Assess the morphology of the erythrocytes.
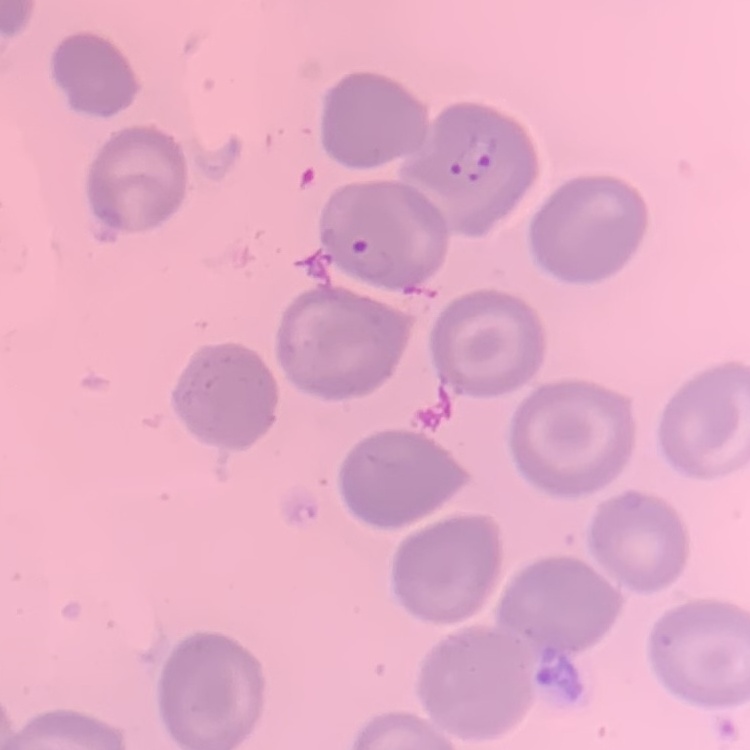
No rouleaux formation.

Summary:
  - Preparation: thin blood film
  - Image type: square crop of a larger photomicrograph
  - Stain: Field's or Giemsa